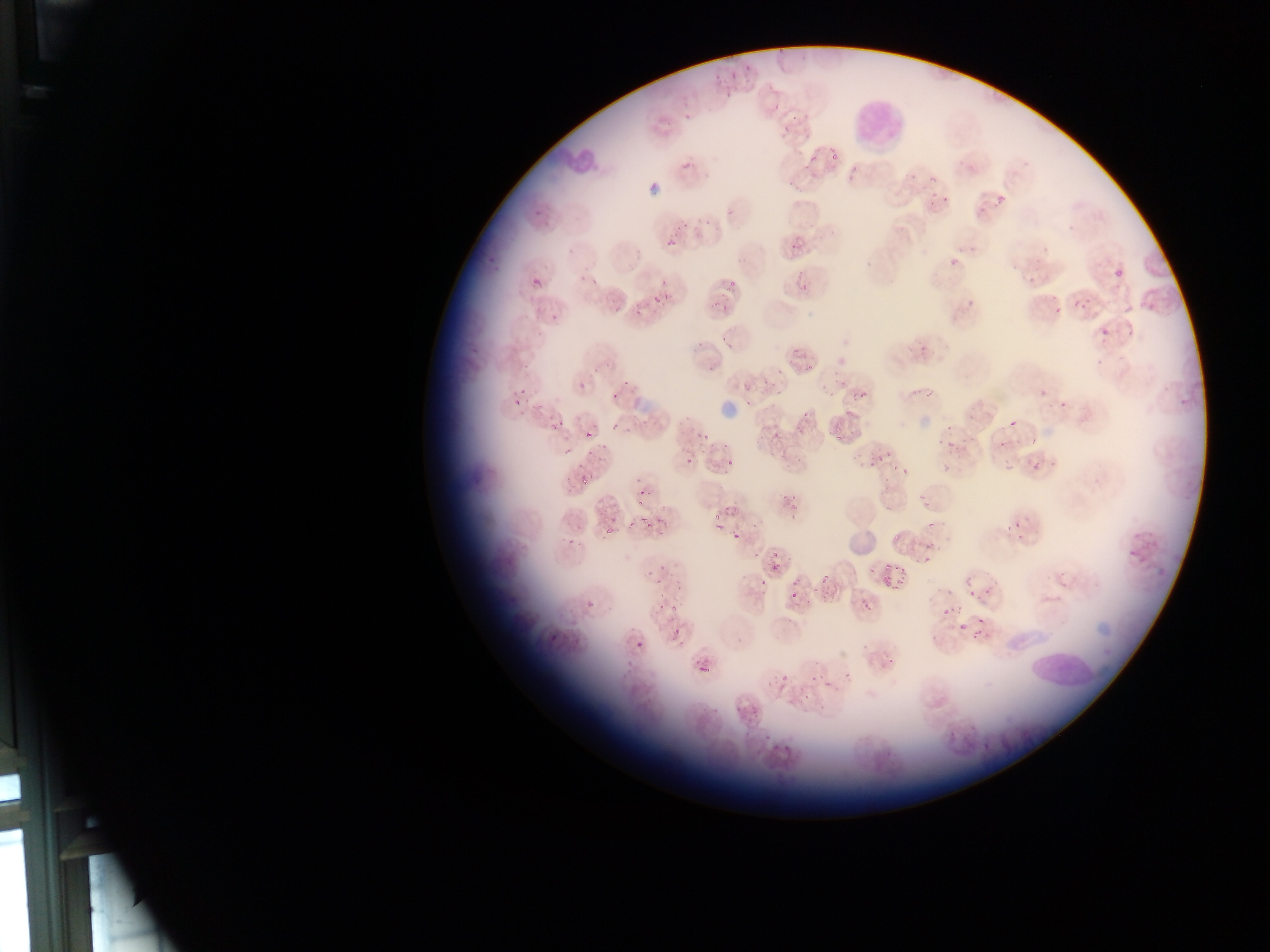

Approximate bounding boxes as {left, top, right, bottom} in pixels.
Summary:
  - Leukocyte locations: {854, 95, 909, 152}, {544, 140, 604, 175}, {1023, 647, 1094, 701}
  - Artifact (stain precipitate or debris) locations: {647, 174, 670, 197}, {717, 398, 738, 421}, {847, 532, 876, 557}, {1086, 612, 1120, 636}
  - Plasmodium parasite locations: {727, 61, 741, 79}, {766, 89, 793, 111}, {780, 123, 795, 133}, {824, 152, 842, 163}, {801, 156, 819, 169}, {923, 175, 941, 185}, {930, 192, 940, 202}, {996, 195, 1005, 204}, {941, 196, 950, 204}, {530, 200, 541, 218}, {671, 213, 695, 244}, {794, 237, 803, 249}, {667, 238, 676, 248}, {628, 248, 641, 266}, {482, 252, 495, 264}, {943, 252, 963, 274}, {1114, 268, 1123, 278}, {589, 270, 600, 288}, {531, 276, 542, 289}, {1027, 277, 1036, 286}, {730, 281, 739, 294}, {710, 285, 727, 307}, {653, 292, 666, 302}, {610, 293, 627, 317}, {1074, 300, 1083, 309}, {632, 303, 645, 323}, {1124, 303, 1134, 313}, {546, 307, 562, 321}, {1101, 327, 1110, 337}, {514, 357, 538, 376}, {804, 357, 817, 377}, {617, 374, 635, 392}, {758, 374, 770, 391}, {576, 380, 592, 390}, {919, 383, 932, 403}, {851, 384, 869, 402}, {607, 387, 625, 401}, {1039, 389, 1048, 399}, {509, 393, 524, 412}, {1055, 396, 1077, 411}, {799, 407, 829, 419}, {551, 419, 563, 431}, {696, 419, 716, 442}, {1010, 419, 1018, 428}, {610, 421, 621, 433}, {771, 421, 788, 440}, {829, 428, 844, 445}, {584, 429, 594, 441}, {1028, 434, 1045, 454}, {714, 435, 731, 454}, {992, 435, 1010, 450}, {944, 436, 957, 454}, {870, 447, 888, 464}, {562, 448, 571, 458}, {1029, 452, 1049, 472}, {725, 454, 742, 468}, {685, 456, 695, 468}, {894, 461, 907, 479}, {583, 471, 595, 486}, {779, 483, 800, 511}, {919, 493, 929, 508}, {636, 495, 646, 506}, {708, 505, 722, 520}, {882, 505, 893, 515}, {640, 516, 647, 525}, {748, 517, 758, 530}, {656, 518, 668, 530}, {627, 519, 639, 537}, {924, 519, 933, 533}, {715, 523, 723, 532}, {600, 527, 611, 537}, {889, 528, 900, 541}, {731, 532, 741, 541}, {923, 537, 937, 553}, {774, 544, 783, 561}, {914, 551, 931, 566}, {871, 555, 909, 586}, {771, 558, 789, 574}, {656, 565, 673, 580}, {754, 576, 773, 591}, {816, 578, 833, 593}, {783, 581, 805, 599}, {963, 582, 986, 602}, {666, 595, 684, 612}, {862, 599, 879, 613}, {584, 600, 597, 612}, {941, 600, 954, 617}, {544, 615, 559, 645}, {674, 616, 688, 632}, {951, 616, 979, 639}, {629, 636, 644, 650}, {698, 663, 712, 675}, {775, 668, 796, 686}, {803, 670, 820, 682}, {820, 674, 830, 691}, {749, 700, 761, 720}, {758, 734, 770, 744}, {773, 739, 785, 754}
  - Country: Ghana
  - Field of view: single
  - Image size: 1270×952 pixels
  - Capture: mobile-phone photograph through a microscope
  - Preparation: thin blood smear